Classify this cell by malaria status.
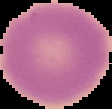

Uninfected.

Segmented cell region on a black background. From a thin blood smear. Image is 112×109 pixels.